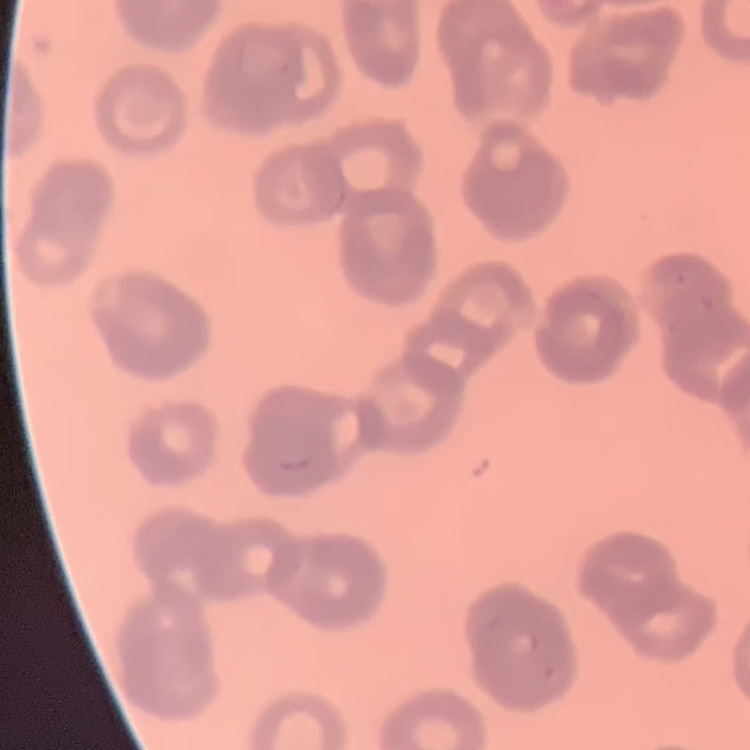

{
  "erythrocyte_morphology": "rouleaux formation",
  "image_type": "one tile cut from a larger photomicrograph",
  "stain": "Field's or Giemsa",
  "preparation": "thin peripheral smear"
}